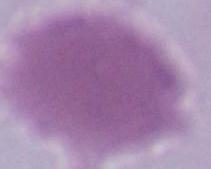

Summary:
  - Magnification: 1000x
  - Identification: red blood cell
  - Modality: micrograph